Assess this cell for malaria.
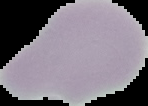

It is uninfected.

Summary:
  - Preparation: thin blood film
  - Image size: 148×106 pixels
  - Image type: cell region segmented out of the field of view; surrounding area masked to black